Assess for malaria.
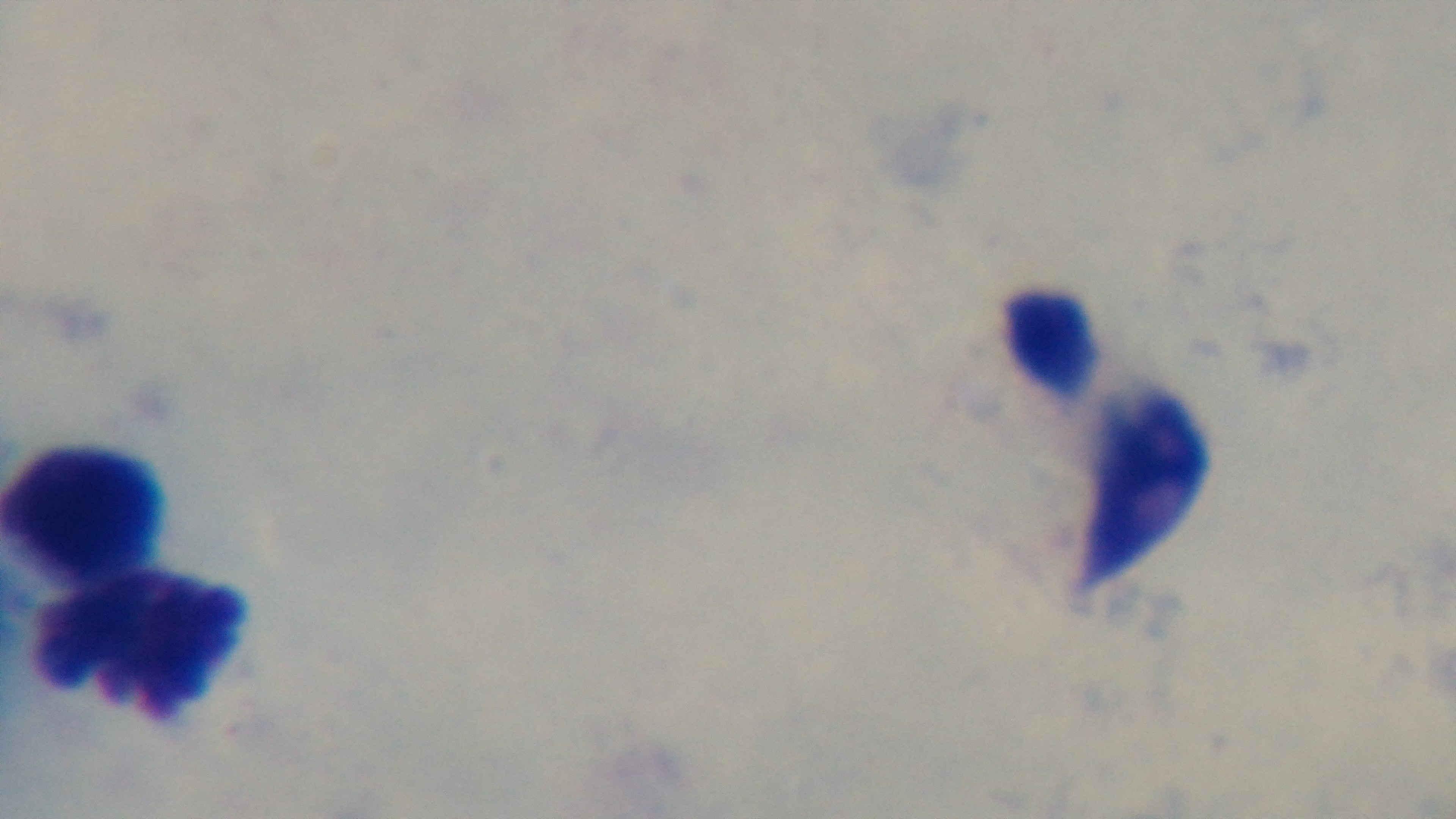
It is uninfected.

Preparation: thick blood film. One field from the slide. 100x oil-immersion objective. Mounted 4K digital camera. Giemsa-stained. Photomicrograph.